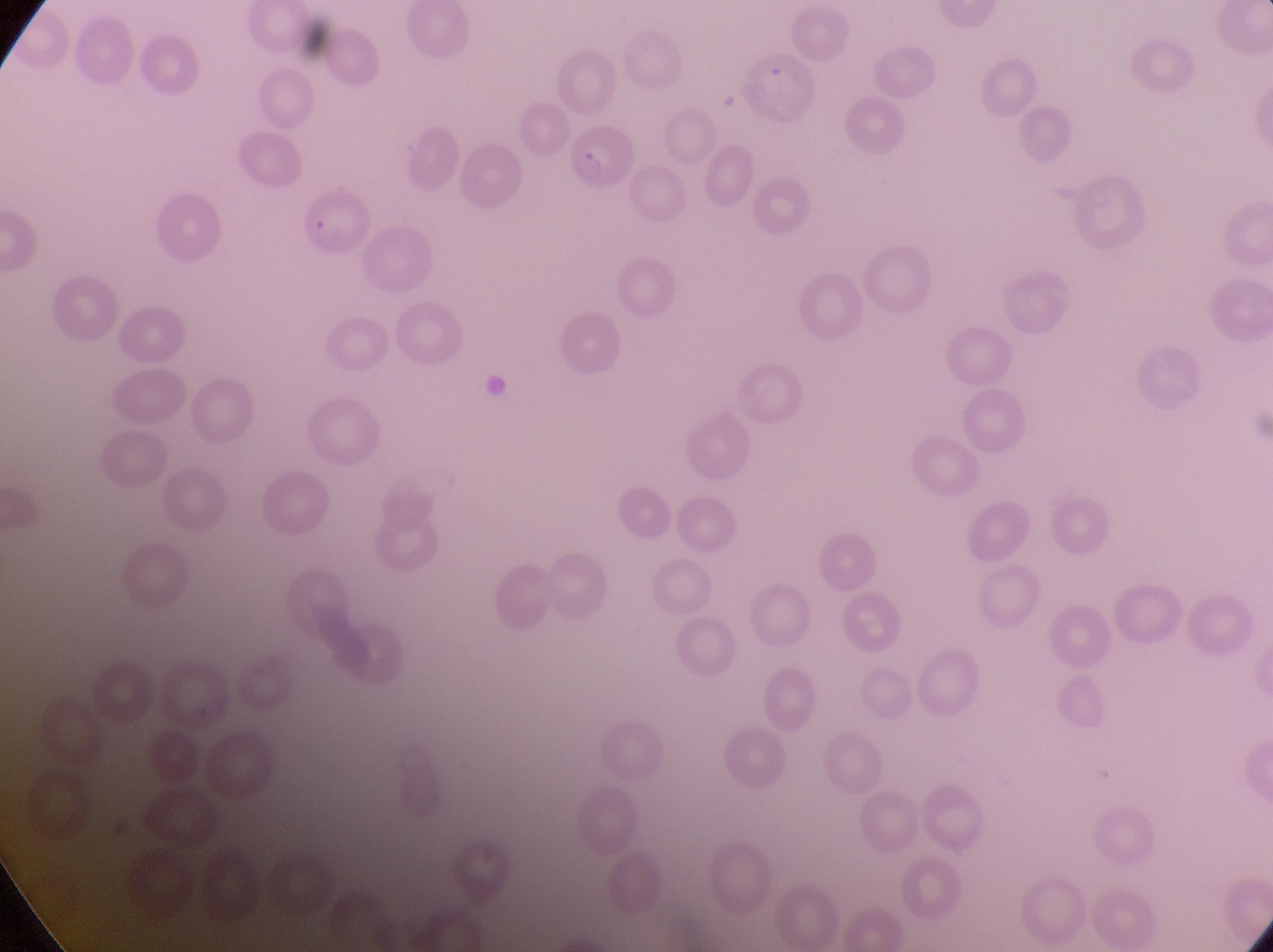

country: Uganda
parasitised_red_blood_cell_locations: 'approximate bounding boxes as {left, top, right, bottom} in pixels: {567, 128, 637, 198}, {295, 192, 375, 257}'
artifact_platelet_like_body_stain_precipitate_or_debris_locations: 'approximate bounding boxes as {left, top, right, bottom} in pixels: {480, 369, 508, 402}'
preparation: thin blood film
magnification: 1000x
field_of_view: single
capture: smartphone photograph through the eyepiece of an Olympus CX-23 microscope
image_size: 1273×952 pixels